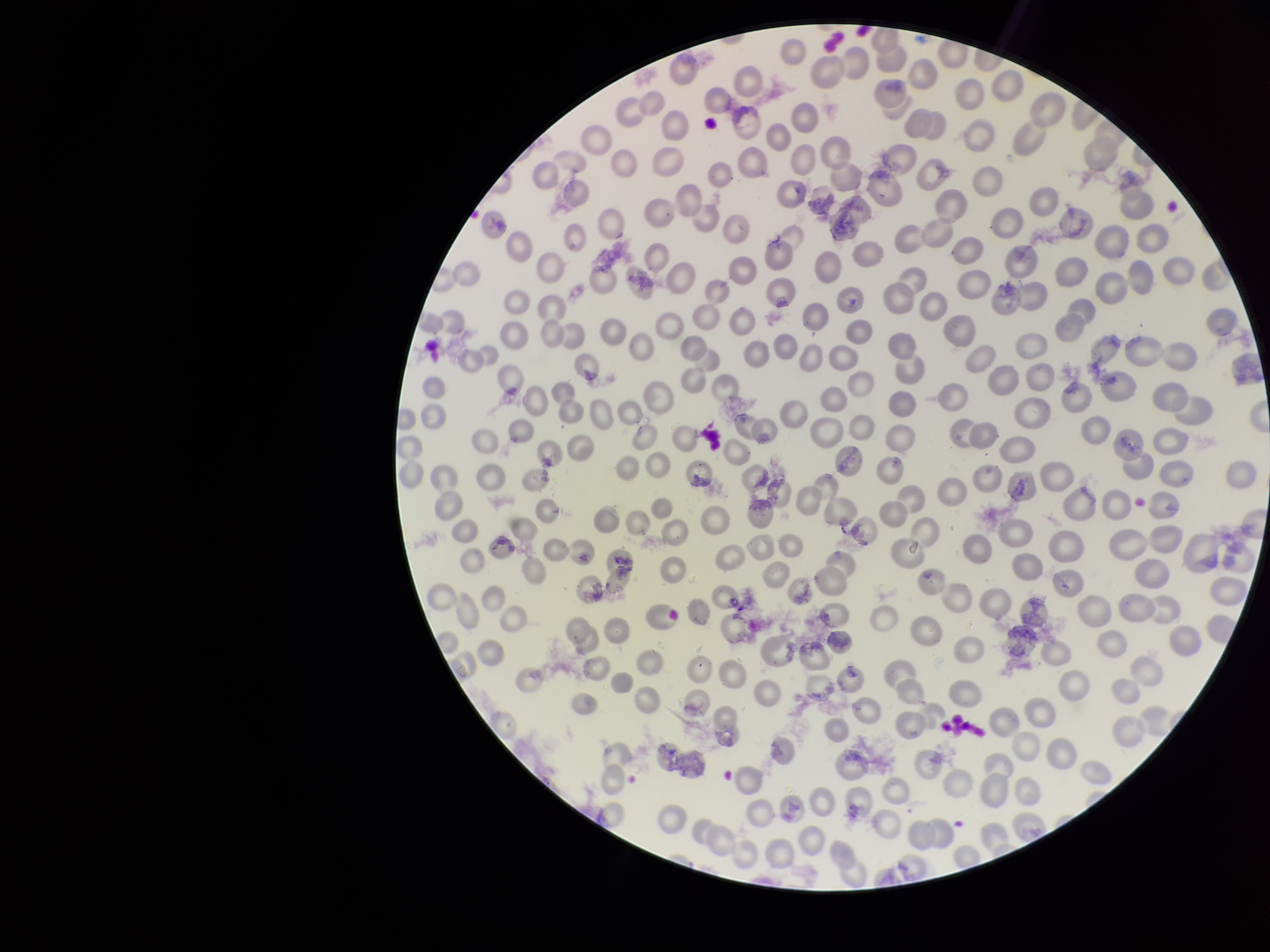
Summary:
  - Capture: smartphone photograph through the microscope eyepiece
  - Field of view: one from this slide
  - Image size: 1270×952 pixels
  - Preparation: thin smear
  - Stain: Giemsa
  - Red blood cell count: 271
  - Patient malaria status: infected
  - Parasitized red blood cells: none identified
  - Parasitized red blood cell count: 0
  - Species reported for this patient: Plasmodium vivax